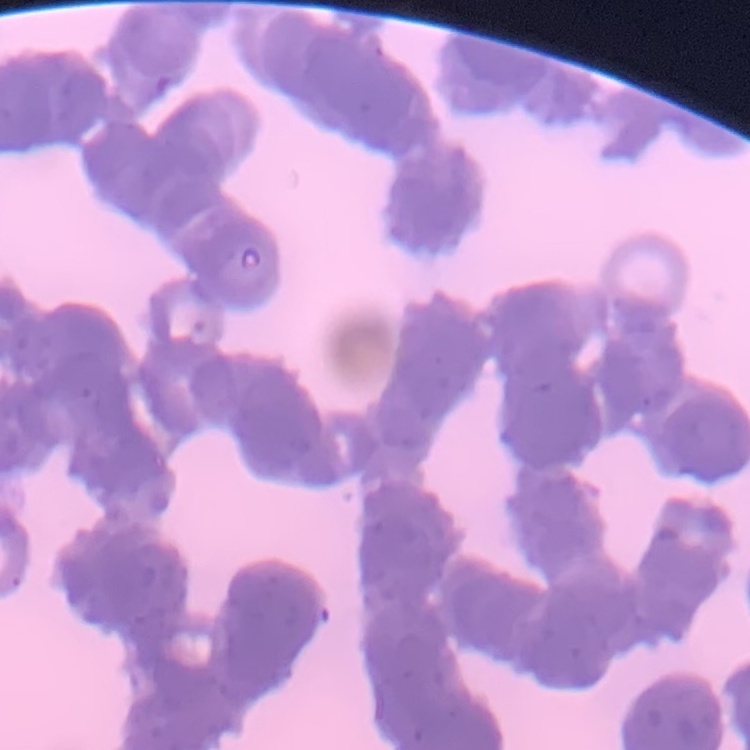
Summary:
  - Red blood cell morphology: rouleaux formation
  - Preparation: thin blood smear
  - Image type: square crop of a larger photomicrograph
  - Stain: Field's or Giemsa